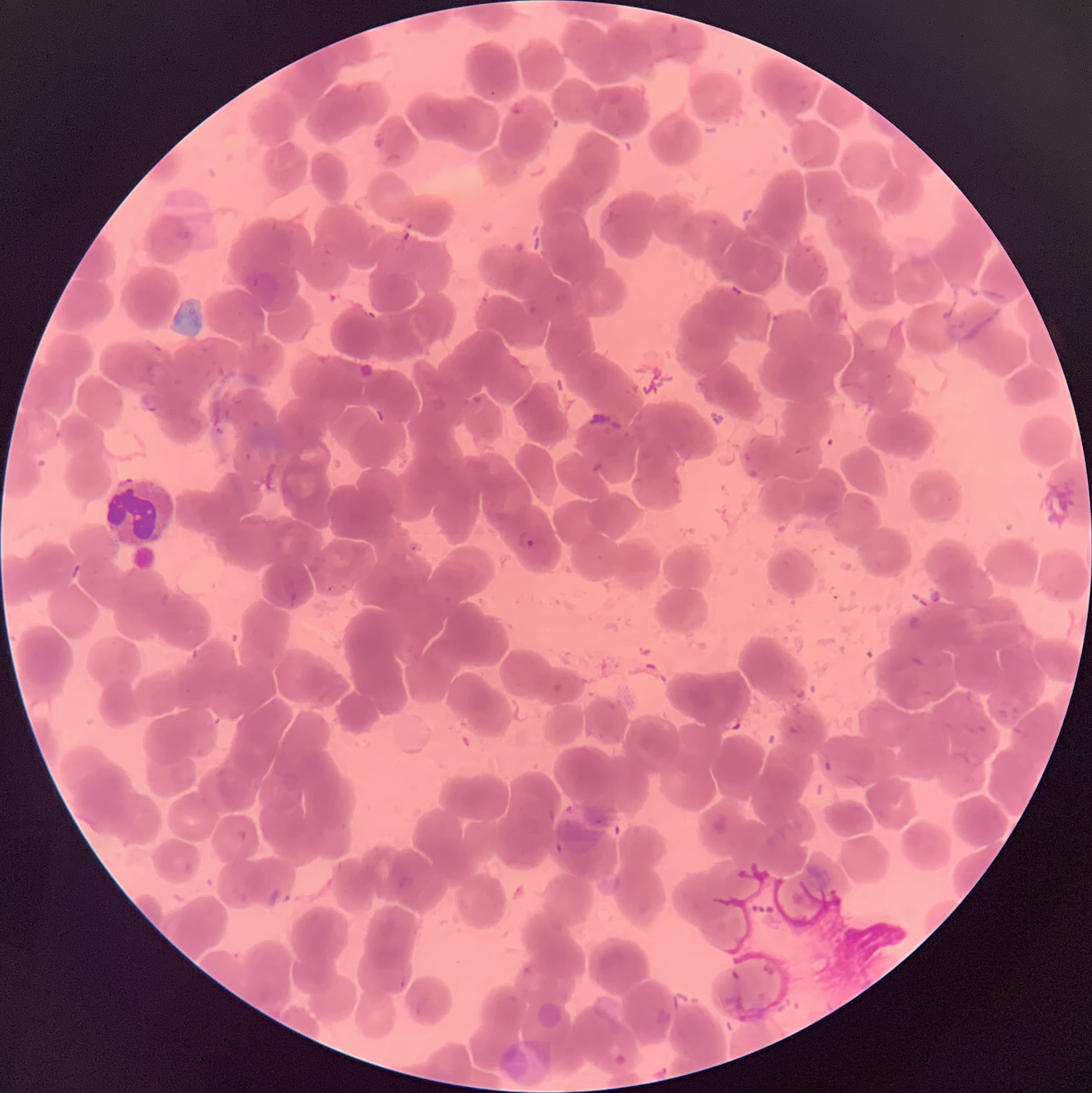
coordinate format = approximate bounding boxes as (x1, y1, x2, y2) in pixels
Plasmodium parasite locations = (517, 529, 536, 551)
red blood cell morphology = rouleaux formation
image size = 1092×1093 pixels
preparation = thin blood film
modality = light microscopy